Classify this cell by malaria status.
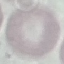

It is uninfected.

capture = smartphone through the microscope eyepiece
image type = automatically extracted cell patch, resized to 64 × 64 pixels
preparation = thin blood smear
stain = Giemsa